Assess this cell for malaria.
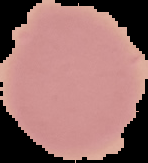
Uninfected.

Summary:
  - Image type: segmented cell region with the area outside set to black
  - Preparation: thin blood film
  - Image size: 148×163 pixels